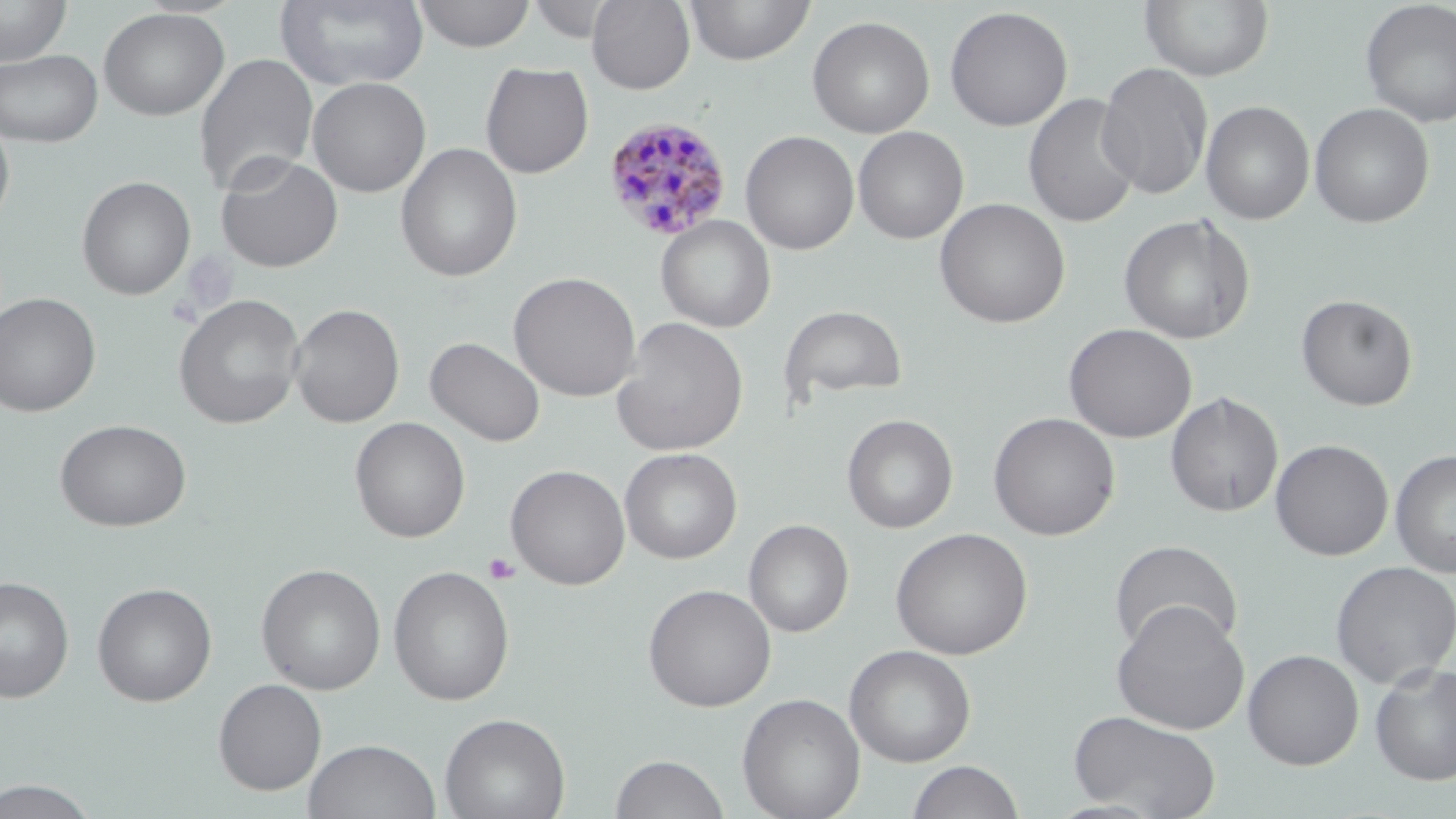
Summary:
  - Coordinate format: approximate bounding boxes as named x1/y1/x2/y2 corners in pixels
  - Plasmodium malariae-infected red blood cell locations: (x1=602, y1=115, x2=733, y2=241)
  - Uninfected red blood cell locations: (x1=275, y1=0, x2=430, y2=91), (x1=412, y1=0, x2=535, y2=52), (x1=586, y1=0, x2=695, y2=94), (x1=685, y1=0, x2=815, y2=66), (x1=1140, y1=0, x2=1274, y2=82), (x1=0, y1=1, x2=72, y2=66), (x1=525, y1=1, x2=623, y2=43), (x1=1360, y1=1, x2=1456, y2=128), (x1=944, y1=5, x2=1074, y2=131), (x1=97, y1=8, x2=230, y2=121), (x1=807, y1=15, x2=935, y2=138), (x1=0, y1=49, x2=103, y2=147), (x1=193, y1=52, x2=319, y2=195), (x1=480, y1=61, x2=594, y2=179), (x1=1097, y1=62, x2=1213, y2=199), (x1=307, y1=77, x2=431, y2=197), (x1=1023, y1=92, x2=1142, y2=228), (x1=1200, y1=100, x2=1314, y2=225), (x1=1309, y1=102, x2=1435, y2=229), (x1=0, y1=115, x2=15, y2=233), (x1=853, y1=126, x2=969, y2=244), (x1=740, y1=130, x2=859, y2=255), (x1=395, y1=143, x2=523, y2=282), (x1=215, y1=152, x2=343, y2=272), (x1=77, y1=176, x2=196, y2=300), (x1=934, y1=198, x2=1071, y2=328), (x1=1118, y1=214, x2=1256, y2=345), (x1=655, y1=216, x2=776, y2=333), (x1=508, y1=272, x2=641, y2=401), (x1=0, y1=292, x2=101, y2=417), (x1=173, y1=294, x2=305, y2=429), (x1=1296, y1=294, x2=1418, y2=411), (x1=288, y1=303, x2=404, y2=428), (x1=779, y1=305, x2=908, y2=404), (x1=612, y1=316, x2=749, y2=456), (x1=1063, y1=323, x2=1197, y2=443), (x1=425, y1=336, x2=545, y2=447), (x1=1166, y1=391, x2=1283, y2=517), (x1=988, y1=411, x2=1121, y2=541), (x1=842, y1=414, x2=958, y2=534), (x1=350, y1=416, x2=470, y2=543), (x1=55, y1=419, x2=192, y2=532), (x1=1270, y1=439, x2=1394, y2=561), (x1=620, y1=447, x2=742, y2=564), (x1=1390, y1=449, x2=1456, y2=579), (x1=505, y1=464, x2=630, y2=590), (x1=744, y1=519, x2=854, y2=637), (x1=890, y1=527, x2=1033, y2=660), (x1=1109, y1=539, x2=1243, y2=656), (x1=1330, y1=560, x2=1456, y2=689), (x1=256, y1=563, x2=386, y2=695), (x1=388, y1=565, x2=515, y2=706), (x1=0, y1=576, x2=74, y2=703), (x1=92, y1=582, x2=217, y2=706), (x1=642, y1=583, x2=776, y2=712), (x1=1110, y1=601, x2=1250, y2=735), (x1=844, y1=644, x2=976, y2=767), (x1=1243, y1=649, x2=1364, y2=769), (x1=1370, y1=661, x2=1456, y2=786), (x1=213, y1=678, x2=327, y2=796), (x1=736, y1=692, x2=865, y2=819), (x1=1068, y1=709, x2=1221, y2=818), (x1=439, y1=712, x2=570, y2=819), (x1=303, y1=738, x2=441, y2=819), (x1=610, y1=753, x2=729, y2=819), (x1=906, y1=760, x2=1025, y2=819), (x1=1, y1=778, x2=100, y2=818)
  - Platelet locations: (x1=483, y1=553, x2=520, y2=585)
  - Slide-level diagnosis: Plasmodium malariae
  - Image size: 1456×819 pixels
  - Preparation: thin blood smear
  - Stain: May-Grünwald-Giemsa
  - Field of view: single
  - Magnification: 1000x
  - Modality: light microscopy